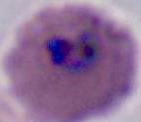
magnification = 400x or 1000x
identification = Plasmodium
modality = photomicrograph